Point out each Plasmodium parasite.
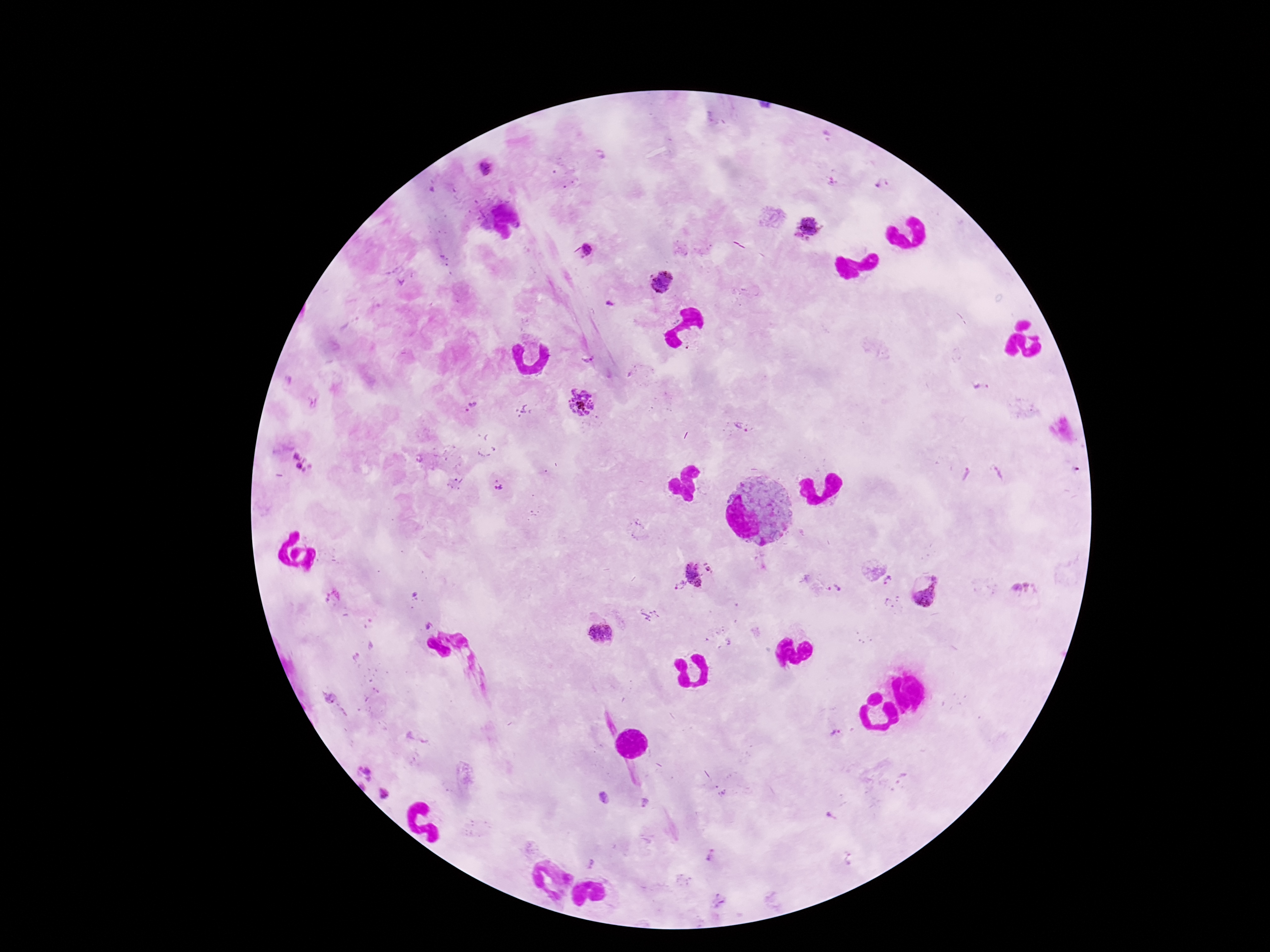
Approximate centers as [x, y] in pixels.
Plasmodium parasites: [486, 168], [881, 184], [810, 225], [586, 251], [663, 283], [609, 303], [587, 358], [579, 403], [472, 406], [742, 428], [302, 462], [497, 486], [708, 566], [695, 574], [887, 581], [678, 584], [835, 589], [1022, 589], [926, 590], [891, 603], [428, 626], [601, 636], [836, 734], [366, 772], [363, 786], [383, 794], [604, 797], [645, 802], [831, 816], [711, 855], [590, 864].

100x magnification. Thick peripheral-blood smear. One field from this slide. Smartphone photograph taken through the microscope eyepiece. Patient malaria status: infected. Image is 1270×952 pixels. Giemsa stain.